Name the parasite shown.
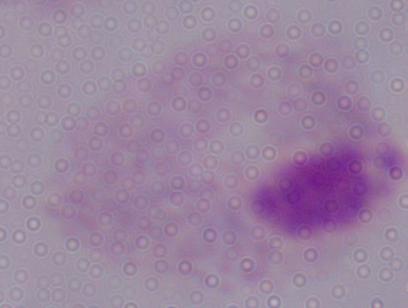
A trichomonad.

Summary:
  - Magnification: 1000x
  - Modality: photomicrograph